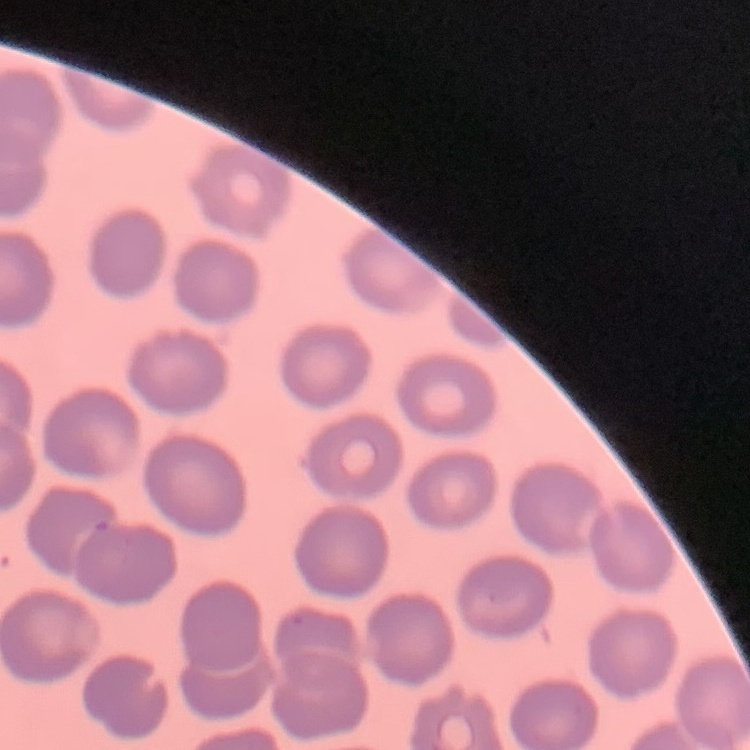

Summary:
  - Erythrocyte morphology: no rouleaux formation
  - Preparation: thin blood smear
  - Image type: square crop of a larger photomicrograph
  - Stain: Field's or Giemsa